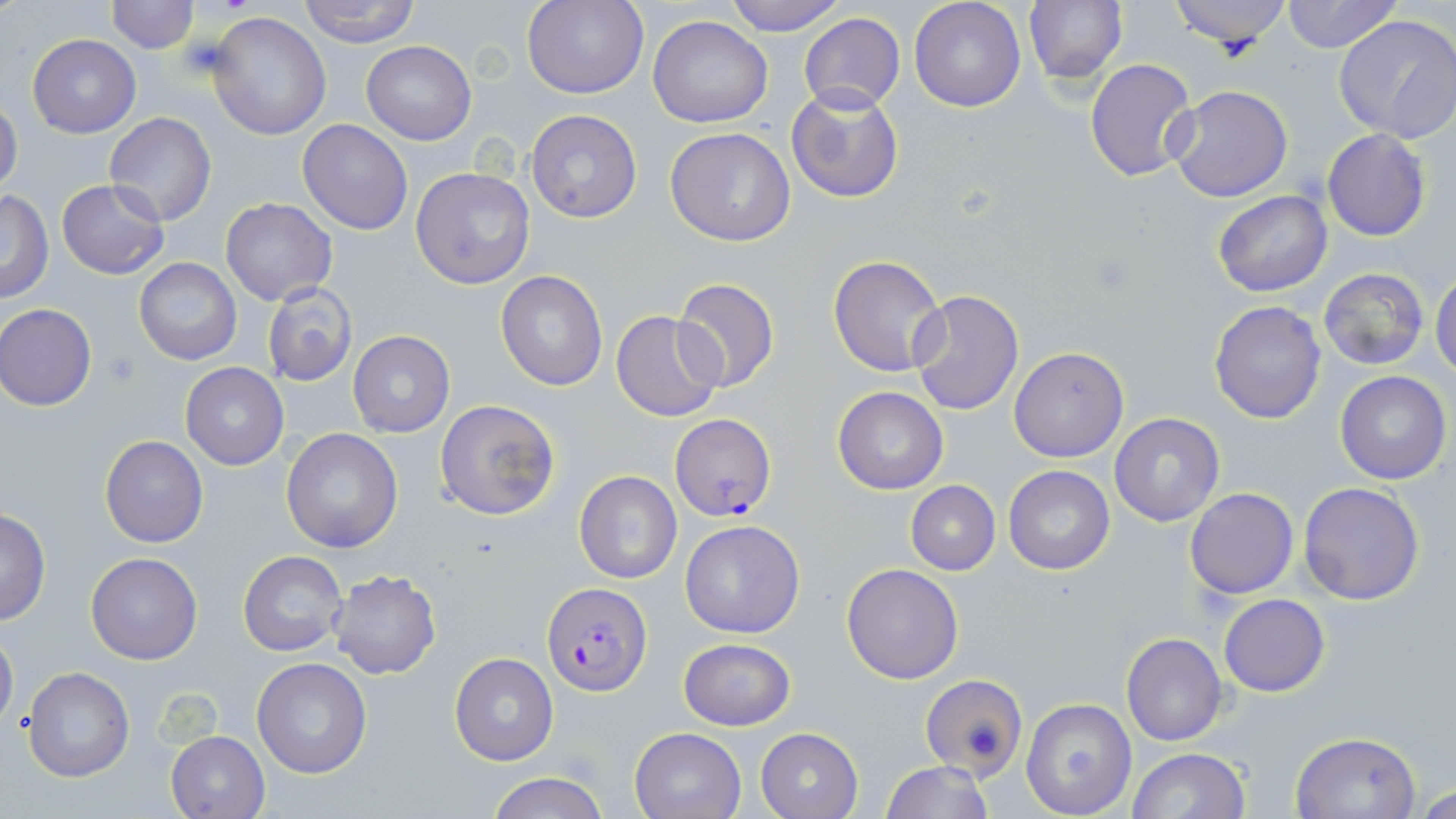

slide_level_diagnosis: Plasmodium falciparum
image_size: 1456×819 pixels
magnification: 1000x
preparation: thin blood film
field_of_view: single
modality: optical microscopy
uninfected_red_blood_cell_locations: 'approximate bounding boxes as (x1, y1, x2, y2) in pixels: (105, 0, 200, 53), (298, 0, 421, 47), (522, 0, 648, 100), (723, 0, 846, 35), (909, 0, 1027, 112), (1169, 0, 1290, 55), (1281, 0, 1400, 54), (1022, 1, 1127, 87), (205, 11, 332, 141), (799, 12, 906, 113), (1332, 12, 1456, 143), (648, 16, 774, 128), (27, 34, 141, 138), (361, 41, 477, 145), (1083, 58, 1199, 183), (786, 85, 904, 204), (1166, 85, 1294, 204), (0, 98, 24, 199), (525, 109, 642, 225), (103, 112, 216, 227), (297, 119, 414, 236), (665, 126, 795, 246), (1321, 129, 1431, 241), (410, 164, 536, 290), (56, 178, 170, 280), (1212, 188, 1332, 297), (1, 190, 54, 304), (220, 197, 338, 305), (827, 253, 947, 377), (133, 257, 241, 366), (1317, 266, 1430, 372), (495, 269, 609, 392), (1430, 269, 1456, 382), (673, 277, 781, 394), (262, 283, 357, 386), (909, 294, 1023, 416), (1209, 301, 1328, 424), (0, 303, 97, 411), (611, 310, 724, 423), (348, 330, 455, 439), (1007, 347, 1128, 462), (180, 362, 289, 470), (1334, 370, 1451, 484), (832, 386, 948, 494), (434, 398, 559, 521), (1109, 413, 1225, 527), (281, 428, 402, 553), (99, 434, 208, 548), (1003, 466, 1114, 576), (573, 469, 682, 585), (905, 480, 1000, 575), (1297, 482, 1425, 606), (1184, 487, 1299, 598), (0, 508, 51, 627), (679, 520, 806, 639), (239, 550, 348, 658), (85, 551, 202, 665), (842, 563, 963, 684), (328, 569, 442, 679), (1218, 594, 1329, 696), (0, 624, 18, 736), (1121, 632, 1228, 746), (677, 638, 797, 731), (449, 652, 559, 766), (251, 657, 373, 779), (22, 666, 134, 781), (919, 674, 1027, 778), (1022, 698, 1136, 818), (628, 726, 748, 819), (754, 727, 864, 819), (1289, 730, 1420, 818), (166, 731, 270, 818), (1127, 747, 1250, 819), (879, 760, 993, 818), (485, 770, 609, 819), (1415, 782, 1456, 819)'
plasmodium_falciparum_infected_red_blood_cell_locations: 'approximate bounding boxes as (x1, y1, x2, y2) in pixels: (670, 414, 776, 521), (541, 583, 651, 695)'
platelet_locations: 'approximate bounding boxes as (x1, y1, x2, y2) in pixels: (175, 34, 235, 77), (103, 351, 142, 388)'
stain: May-Grünwald-Giemsa